Assess this cell for malaria.
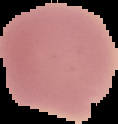
Uninfected.

image type = segmented cell region on a black background
preparation = thin blood smear
image size = 118×124 pixels